Locate and identify every blood parasite.
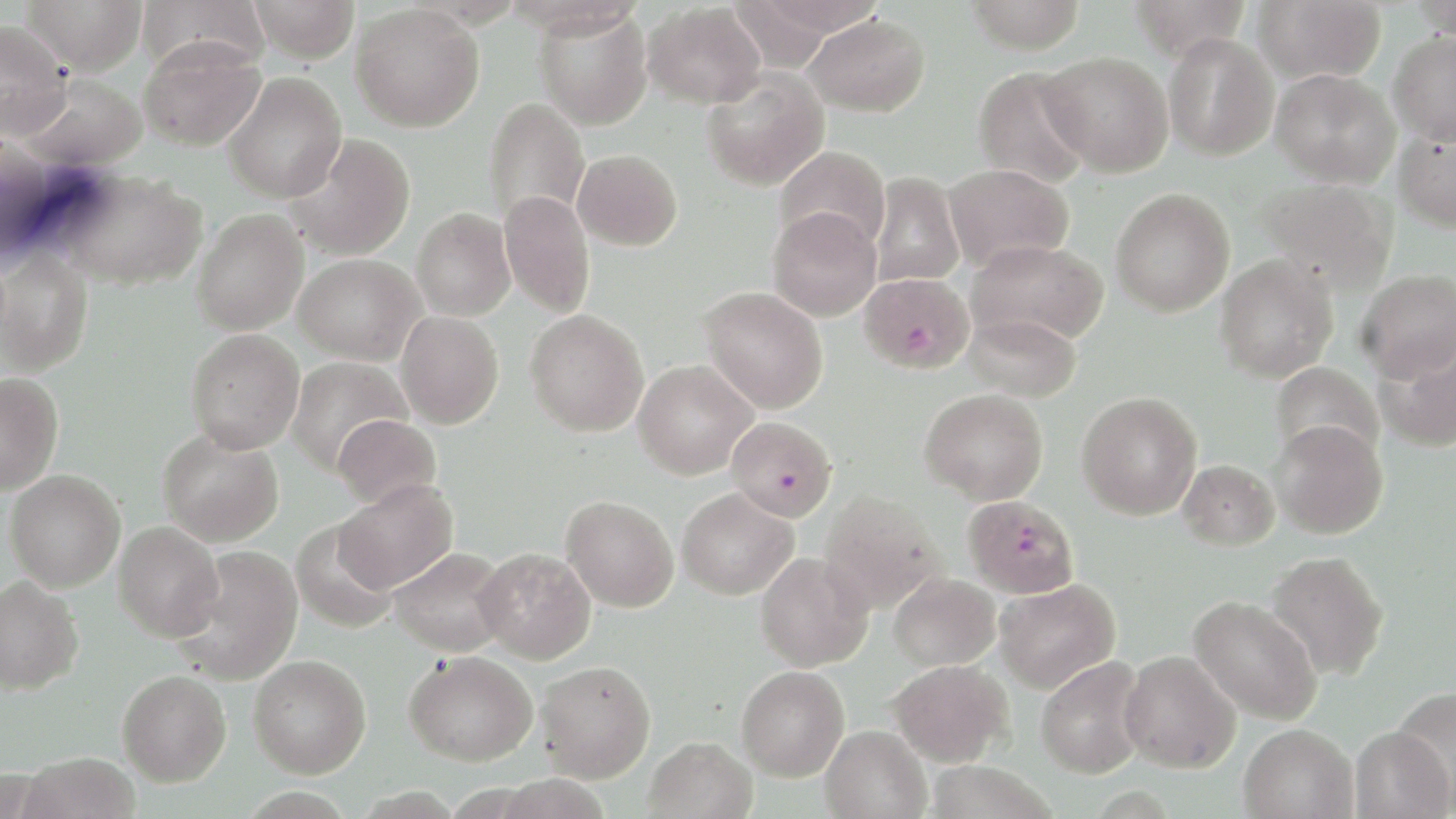

Approximate bounding boxes as [x1, y1, x2, y2] in pixels.
Plasmodium falciparum-infected red blood cells: [861, 272, 973, 374], [726, 415, 837, 522], [963, 495, 1079, 598].
No Plasmodium ovale, Plasmodium malariae, Plasmodium vivax, Babesia divergens, or Trypanosoma brucei observed.

Summary:
  - Uninfected red blood cell locations: [22, 0, 147, 75], [137, 0, 267, 76], [248, 0, 360, 63], [963, 0, 1086, 54], [1128, 0, 1252, 59], [1252, 0, 1386, 84], [643, 2, 766, 109], [350, 4, 484, 132], [535, 9, 653, 131], [804, 12, 930, 117], [0, 19, 71, 138], [1387, 31, 1456, 145], [1163, 32, 1279, 161], [138, 37, 265, 151], [1040, 51, 1173, 176], [972, 65, 1093, 190], [700, 68, 829, 191], [1271, 68, 1400, 188], [223, 71, 347, 203], [18, 73, 150, 170], [483, 97, 589, 226], [1393, 123, 1456, 232], [284, 133, 414, 260], [775, 146, 891, 254], [573, 149, 682, 251], [944, 164, 1074, 273], [59, 170, 208, 291], [869, 172, 965, 287], [1257, 178, 1398, 295], [1110, 187, 1235, 317], [499, 190, 596, 318], [767, 207, 882, 321], [412, 208, 515, 320], [191, 209, 309, 335], [966, 239, 1108, 348], [0, 248, 93, 377], [294, 253, 425, 365], [1214, 254, 1339, 383], [1357, 269, 1456, 382], [700, 286, 828, 414], [525, 309, 649, 437], [395, 311, 503, 429], [963, 313, 1082, 402], [185, 328, 305, 454], [1375, 339, 1456, 454], [286, 355, 412, 474], [633, 360, 758, 479], [1270, 362, 1384, 464], [0, 372, 62, 495], [920, 388, 1048, 504], [1077, 392, 1202, 520], [332, 414, 442, 510], [1270, 421, 1388, 539], [157, 427, 284, 547], [1178, 459, 1279, 550], [5, 470, 126, 592], [334, 479, 458, 593], [676, 487, 798, 600], [819, 490, 948, 614], [561, 495, 679, 612], [113, 521, 224, 642], [290, 521, 400, 634], [172, 545, 303, 685], [387, 546, 512, 657], [474, 547, 596, 663], [1264, 550, 1390, 681], [755, 552, 873, 672], [889, 572, 1001, 670], [0, 575, 85, 695], [994, 578, 1121, 694], [1188, 596, 1323, 725], [404, 650, 537, 766], [1118, 650, 1241, 773], [248, 654, 371, 777], [1035, 656, 1149, 779], [887, 659, 1013, 767], [535, 660, 656, 782], [736, 665, 849, 781], [117, 669, 232, 787], [1391, 684, 1456, 810], [1238, 722, 1357, 819], [821, 725, 931, 819], [1350, 725, 1453, 819], [642, 736, 758, 819], [19, 752, 141, 819]
  - Slide-level diagnosis: Plasmodium falciparum
  - Field of view: one of a larger specimen
  - Magnification: 1000x
  - Image size: 1456×819 pixels
  - Stain: May-Grünwald-Giemsa
  - Modality: optical microscopy
  - Preparation: thin blood smear